Give a bounding box for every parasitised red blood cell.
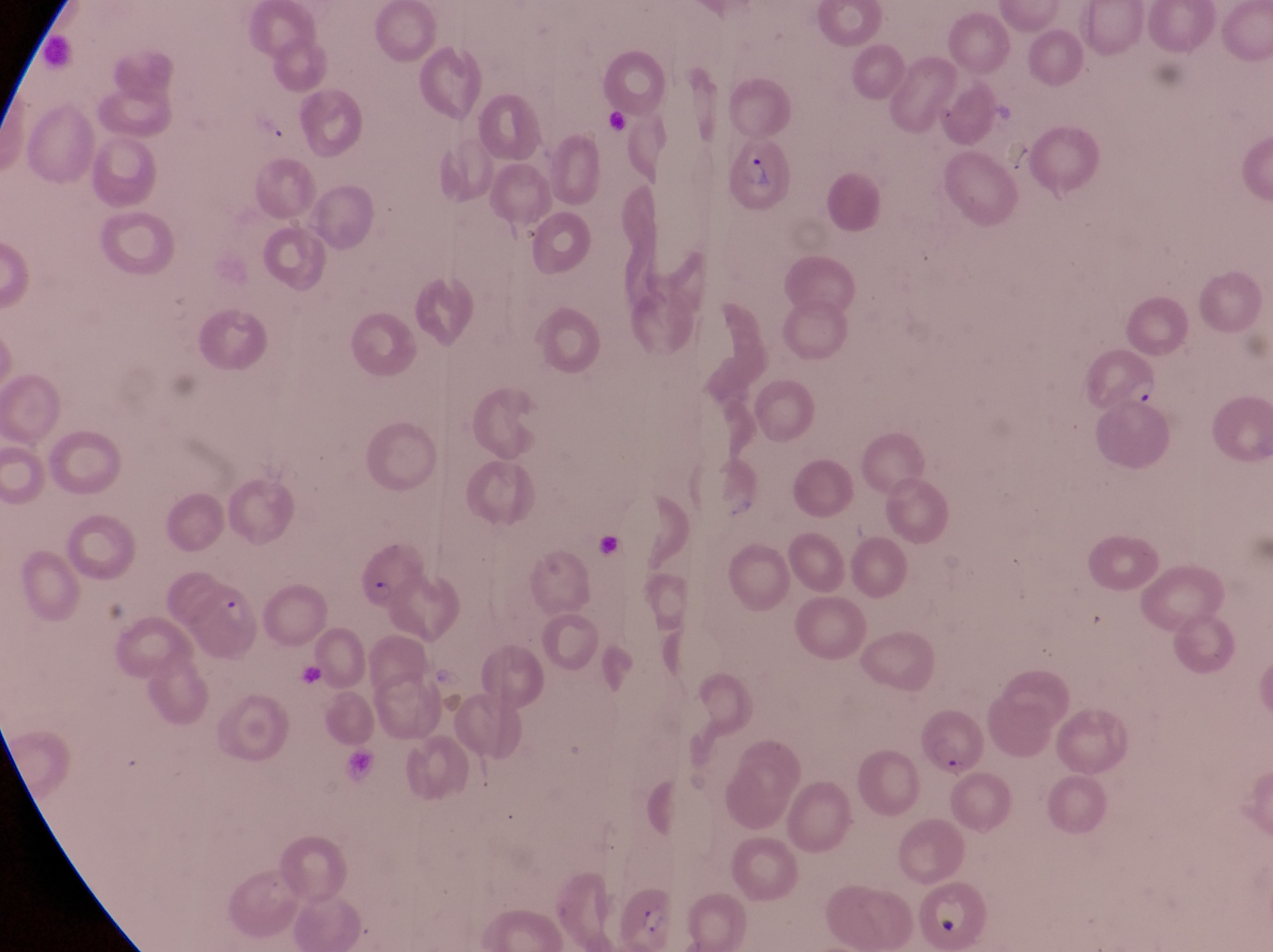

Approximate bounding boxes as left top right bottom in pixels.
Parasitised red blood cells: 731 140 794 215; 1078 348 1165 415; 356 550 419 615; 917 705 987 782; 617 884 672 950.

Magnification of 1000x. Thin blood film. Image is 1273×952 pixels. Sample from Uganda. Captured by a smartphone held over the eyepiece of an Olympus CX-23 microscope. One field of view.